Classify this cell by malaria status.
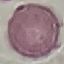

Uninfected.

Summary:
  - Image type: cell patch, automatically extracted from a larger field of view and resized to 64 × 64 pixels
  - Capture: smartphone through the microscope eyepiece
  - Stain: Giemsa
  - Preparation: thin blood film